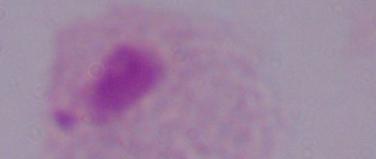 Photomicrograph. A trichomonad is seen. 1000x magnification.